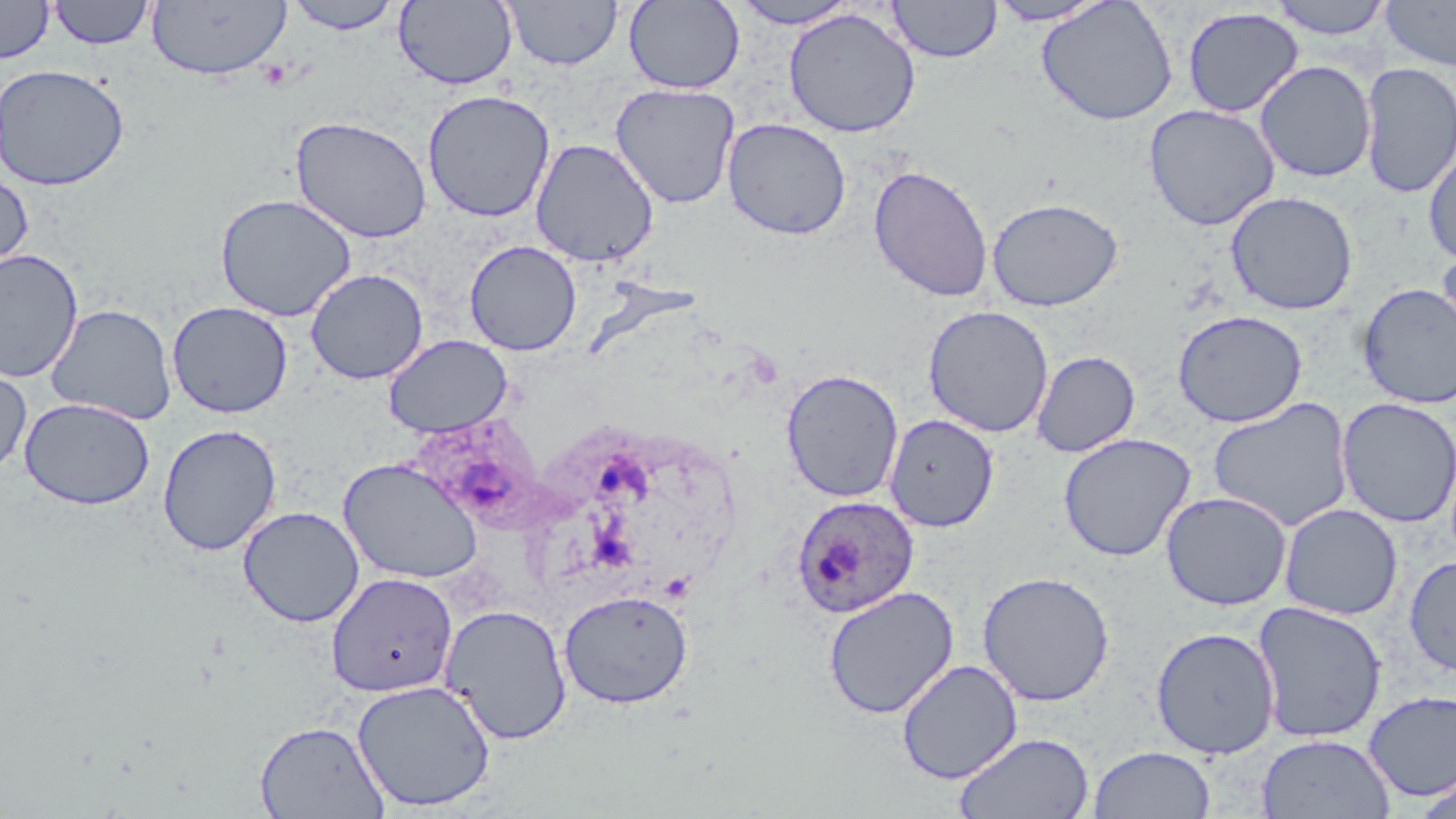

{
  "slide_level_diagnosis": "Plasmodium ovale",
  "field_of_view": "one of a larger specimen",
  "uninfected_red_blood_cell_locations": "approximate bounding boxes as named x1/y1/x2/y2 corners in pixels: (x1=284, y1=0, x2=403, y2=34), (x1=504, y1=0, x2=623, y2=70), (x1=985, y1=0, x2=1113, y2=26), (x1=1036, y1=0, x2=1179, y2=126), (x1=1267, y1=0, x2=1393, y2=39), (x1=0, y1=1, x2=55, y2=63), (x1=48, y1=1, x2=155, y2=49), (x1=146, y1=1, x2=291, y2=80), (x1=394, y1=1, x2=518, y2=91), (x1=624, y1=1, x2=745, y2=94), (x1=729, y1=1, x2=862, y2=29), (x1=887, y1=1, x2=1002, y2=63), (x1=1380, y1=1, x2=1456, y2=71), (x1=1181, y1=7, x2=1304, y2=118), (x1=783, y1=8, x2=921, y2=138), (x1=1255, y1=60, x2=1377, y2=183), (x1=1359, y1=62, x2=1456, y2=199), (x1=0, y1=64, x2=130, y2=191), (x1=610, y1=82, x2=741, y2=209), (x1=422, y1=90, x2=556, y2=222), (x1=1144, y1=104, x2=1280, y2=231), (x1=290, y1=115, x2=432, y2=244), (x1=722, y1=117, x2=852, y2=240), (x1=531, y1=139, x2=660, y2=267), (x1=1423, y1=142, x2=1456, y2=267), (x1=868, y1=164, x2=994, y2=302), (x1=0, y1=168, x2=34, y2=278), (x1=1225, y1=191, x2=1359, y2=315), (x1=215, y1=193, x2=357, y2=322), (x1=986, y1=197, x2=1124, y2=311), (x1=464, y1=240, x2=582, y2=356), (x1=1435, y1=242, x2=1455, y2=364), (x1=0, y1=248, x2=83, y2=381), (x1=0, y1=266, x2=144, y2=418), (x1=305, y1=268, x2=428, y2=384), (x1=1357, y1=283, x2=1456, y2=409), (x1=167, y1=301, x2=293, y2=418), (x1=45, y1=303, x2=177, y2=425), (x1=922, y1=305, x2=1054, y2=438), (x1=1172, y1=309, x2=1308, y2=428), (x1=383, y1=334, x2=513, y2=437), (x1=1032, y1=350, x2=1140, y2=457), (x1=0, y1=359, x2=32, y2=477), (x1=781, y1=369, x2=904, y2=503), (x1=1208, y1=396, x2=1354, y2=532), (x1=1336, y1=397, x2=1455, y2=528), (x1=19, y1=398, x2=156, y2=509), (x1=884, y1=414, x2=999, y2=532), (x1=157, y1=423, x2=282, y2=556), (x1=1057, y1=432, x2=1196, y2=562), (x1=338, y1=457, x2=484, y2=584), (x1=1160, y1=491, x2=1292, y2=611), (x1=1279, y1=503, x2=1403, y2=620), (x1=238, y1=506, x2=365, y2=627), (x1=1403, y1=554, x2=1456, y2=677), (x1=977, y1=571, x2=1115, y2=706), (x1=326, y1=572, x2=458, y2=698), (x1=823, y1=585, x2=959, y2=719), (x1=558, y1=589, x2=693, y2=709), (x1=1251, y1=600, x2=1388, y2=744), (x1=440, y1=603, x2=573, y2=745), (x1=1150, y1=626, x2=1281, y2=759), (x1=897, y1=659, x2=1023, y2=784), (x1=352, y1=678, x2=496, y2=812), (x1=1363, y1=690, x2=1456, y2=802), (x1=255, y1=720, x2=389, y2=819), (x1=954, y1=732, x2=1095, y2=819), (x1=1256, y1=733, x2=1395, y2=819), (x1=1088, y1=745, x2=1216, y2=819), (x1=1411, y1=774, x2=1455, y2=819)",
  "preparation": "thin blood film",
  "image_size": "1456×819 pixels",
  "magnification": "1000x",
  "modality": "light microscopy",
  "plasmodium_ovale_infected_red_blood_cell_locations": "approximate bounding boxes as named x1/y1/x2/y2 corners in pixels: (x1=792, y1=494, x2=920, y2=617)",
  "stain": "May-Grünwald-Giemsa"
}